Comment on the morphology of the erythrocytes.
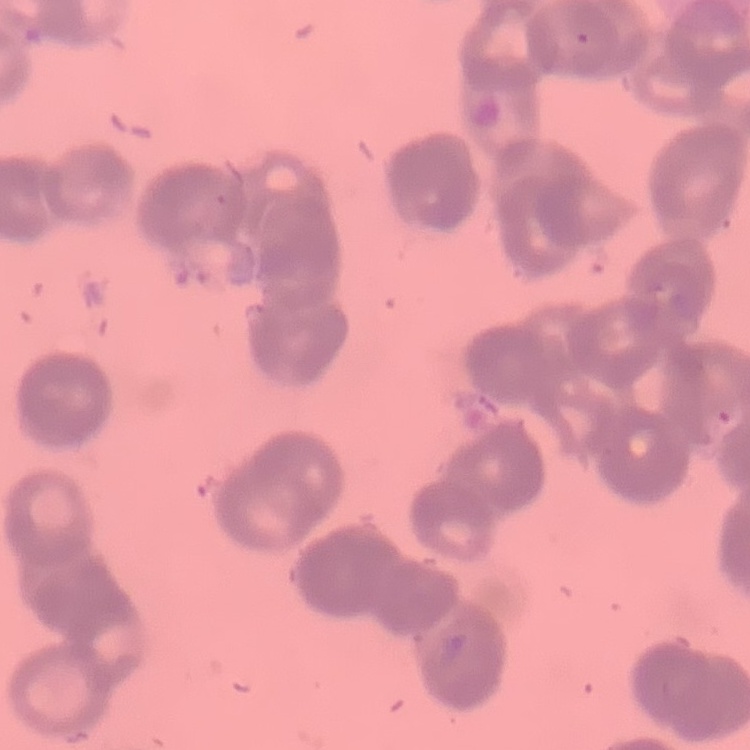

Rouleaux formation.

stain = Field's or Giemsa
preparation = thin peripheral smear
image type = one tile cut from a larger photomicrograph